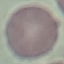

malaria_status: uninfected
stain: Giemsa
capture: smartphone camera at the microscope eyepiece
preparation: thin blood film
image_type: cell patch, automatically extracted from a larger field of view and resized to 64 × 64 pixels